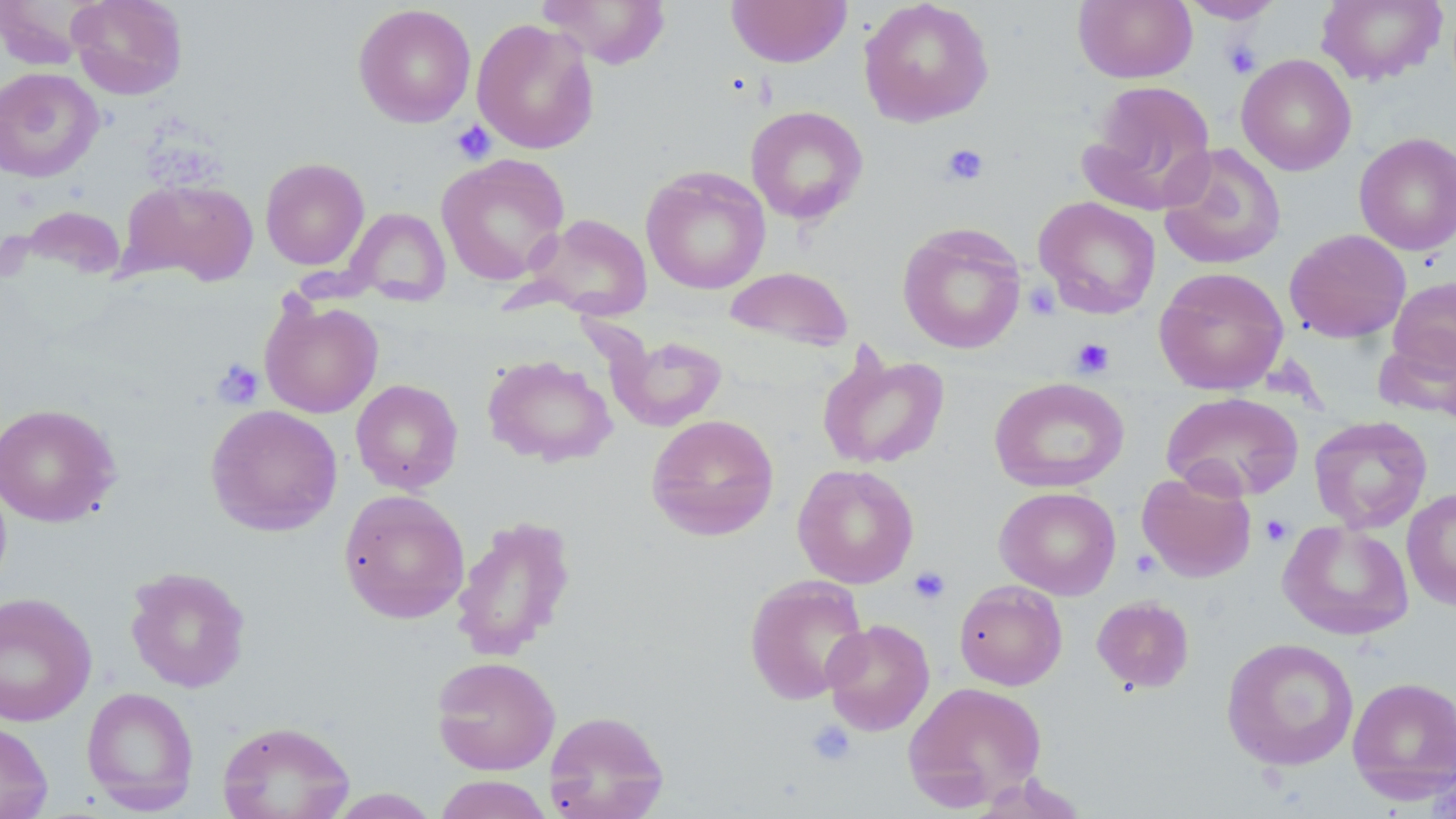

Approximate bounding boxes as (x1,y1)-(x2,y2) corner pairs in pixels. Uninfected red blood cell locations: (67,0)-(188,100), (538,0)-(672,69), (726,0)-(852,67), (859,0)-(995,127), (1073,0)-(1197,84), (1178,0)-(1286,23), (1316,0)-(1448,86), (0,1)-(96,68), (352,4)-(476,127), (471,18)-(599,154), (1236,54)-(1356,176), (0,67)-(103,182), (1082,80)-(1216,213), (745,105)-(869,225), (1354,132)-(1456,256), (1158,143)-(1286,271), (436,154)-(570,285), (260,157)-(370,271), (641,166)-(771,294), (122,178)-(259,286), (1034,196)-(1161,319), (344,207)-(451,306), (529,214)-(653,320), (897,222)-(1027,355), (1284,229)-(1411,343), (724,266)-(854,352), (1154,266)-(1288,396), (1387,276)-(1456,379), (259,294)-(384,419), (606,333)-(727,431), (1375,333)-(1456,423), (816,346)-(950,470), (482,354)-(617,467), (989,377)-(1129,493), (351,378)-(463,494), (1161,391)-(1305,501), (0,403)-(121,527), (205,404)-(343,536), (646,414)-(780,541), (1309,415)-(1432,533), (792,463)-(919,588), (1137,471)-(1257,582), (994,486)-(1121,599), (1401,487)-(1456,611), (338,489)-(470,624), (450,514)-(577,661), (1278,520)-(1414,640), (125,566)-(251,693), (744,574)-(870,705), (954,580)-(1067,690), (0,592)-(97,726), (1092,596)-(1194,693), (822,618)-(935,736), (1222,637)-(1359,771), (431,655)-(561,776), (1347,676)-(1456,805), (903,681)-(1047,809), (81,687)-(199,814), (544,709)-(669,819), (0,720)-(53,819), (217,720)-(356,819), (965,772)-(1089,818), (434,775)-(553,819), (325,788)-(440,818). Platelet locations: (1221,39)-(1262,78), (451,120)-(496,164), (939,143)-(990,186), (1071,337)-(1115,378), (211,358)-(265,409), (1260,515)-(1294,547), (908,566)-(951,605), (806,720)-(856,767). Slide-level diagnosis: negative for blood parasites. May-Grünwald-Giemsa stain. Thin blood film. Captured at 1000x magnification. Light microscopy. Single field of view. Image is 1456×819 pixels.